Give the extent of all Plasmodium ovale-infected red blood cells.
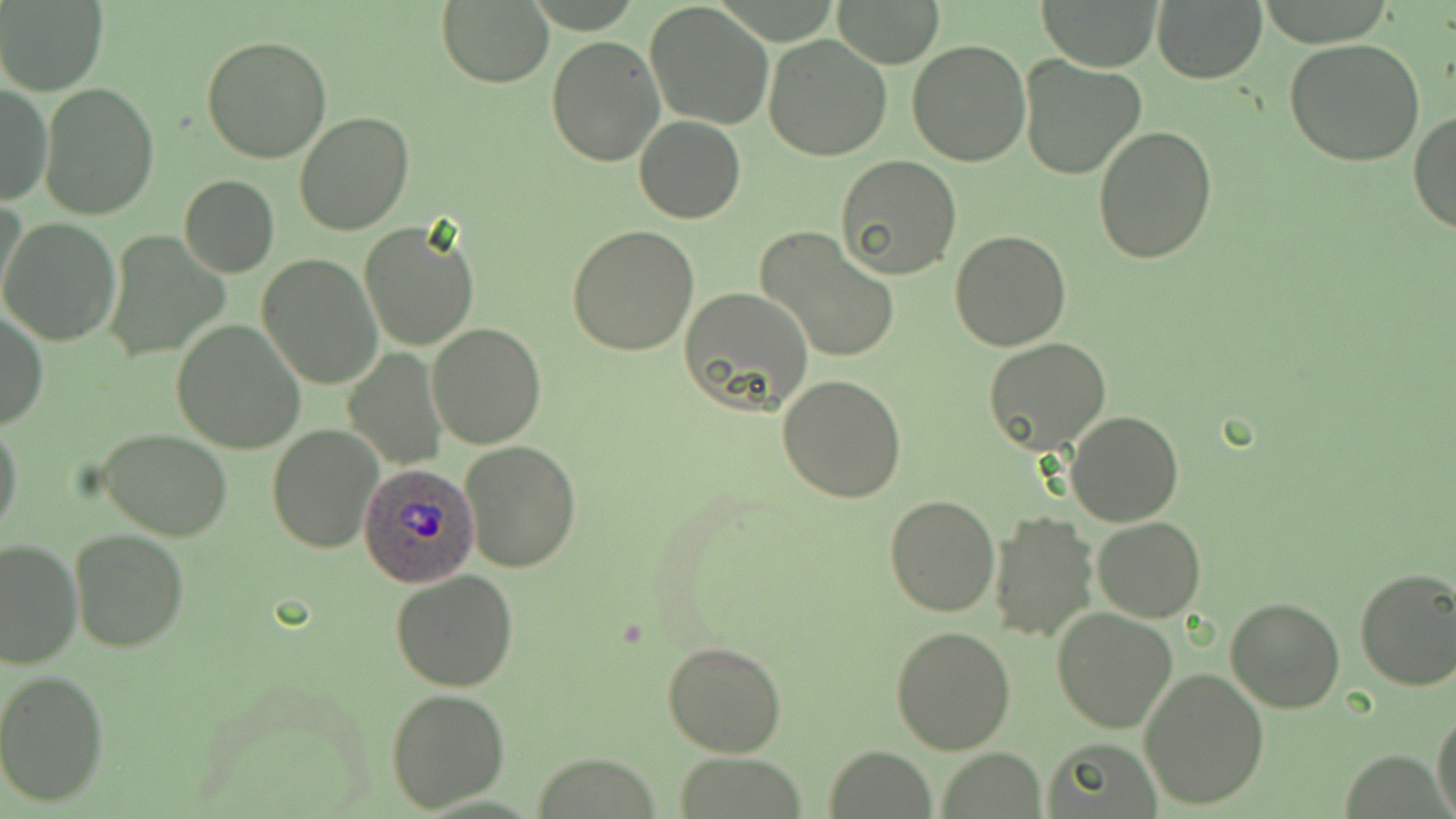

Approximate bounding boxes as [x1, y1, x2, y2] in pixels.
Plasmodium ovale-infected red blood cells: [358, 463, 480, 587].

slide-level diagnosis = Plasmodium ovale
field of view = one of a larger specimen
uninfected red blood cell locations = approximate bounding boxes as [x1, y1, x2, y2] in pixels: [833, 0, 944, 67], [1041, 0, 1162, 72], [2, 1, 107, 93], [644, 1, 772, 129], [1153, 1, 1265, 83], [437, 2, 553, 87], [203, 33, 332, 163], [764, 33, 893, 160], [546, 34, 665, 167], [906, 39, 1031, 168], [1283, 39, 1427, 168], [1018, 55, 1147, 180], [40, 82, 159, 221], [0, 85, 50, 206], [1410, 109, 1456, 234], [295, 111, 414, 235], [634, 116, 745, 224], [1094, 126, 1218, 265], [835, 154, 962, 279], [179, 176, 279, 277], [1, 195, 28, 312], [0, 217, 121, 345], [358, 220, 480, 353], [567, 226, 699, 356], [756, 226, 901, 365], [106, 229, 231, 360], [949, 229, 1071, 351], [257, 253, 383, 388], [681, 286, 813, 414], [0, 308, 47, 431], [171, 320, 306, 453], [427, 322, 546, 448], [983, 338, 1113, 456], [345, 348, 448, 467], [777, 374, 908, 503], [1065, 411, 1183, 527], [0, 420, 23, 539], [266, 424, 383, 554], [97, 428, 234, 540], [461, 440, 581, 572], [882, 494, 1000, 617], [989, 511, 1099, 644], [1092, 516, 1206, 622], [69, 527, 190, 652], [0, 538, 82, 669], [1353, 568, 1456, 693], [390, 569, 521, 693], [1227, 596, 1344, 713], [1052, 606, 1180, 734], [891, 626, 1015, 753], [661, 641, 787, 757], [1139, 668, 1270, 810], [0, 670, 109, 807], [385, 688, 510, 811], [1432, 707, 1456, 819], [1041, 737, 1164, 818], [826, 745, 936, 818], [937, 748, 1047, 817], [673, 753, 806, 818]
stain = May-Grünwald-Giemsa
preparation = thin blood film
modality = light microscopy
image size = 1456×819 pixels
magnification = 1000x